Report the malaria status of this cell.
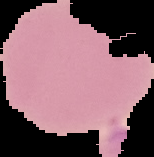

It is uninfected.

Summary:
  - Image size: 154×157 pixels
  - Preparation: thin blood film
  - Image type: segmented cell region with the area outside set to black